Comment on the background quality.
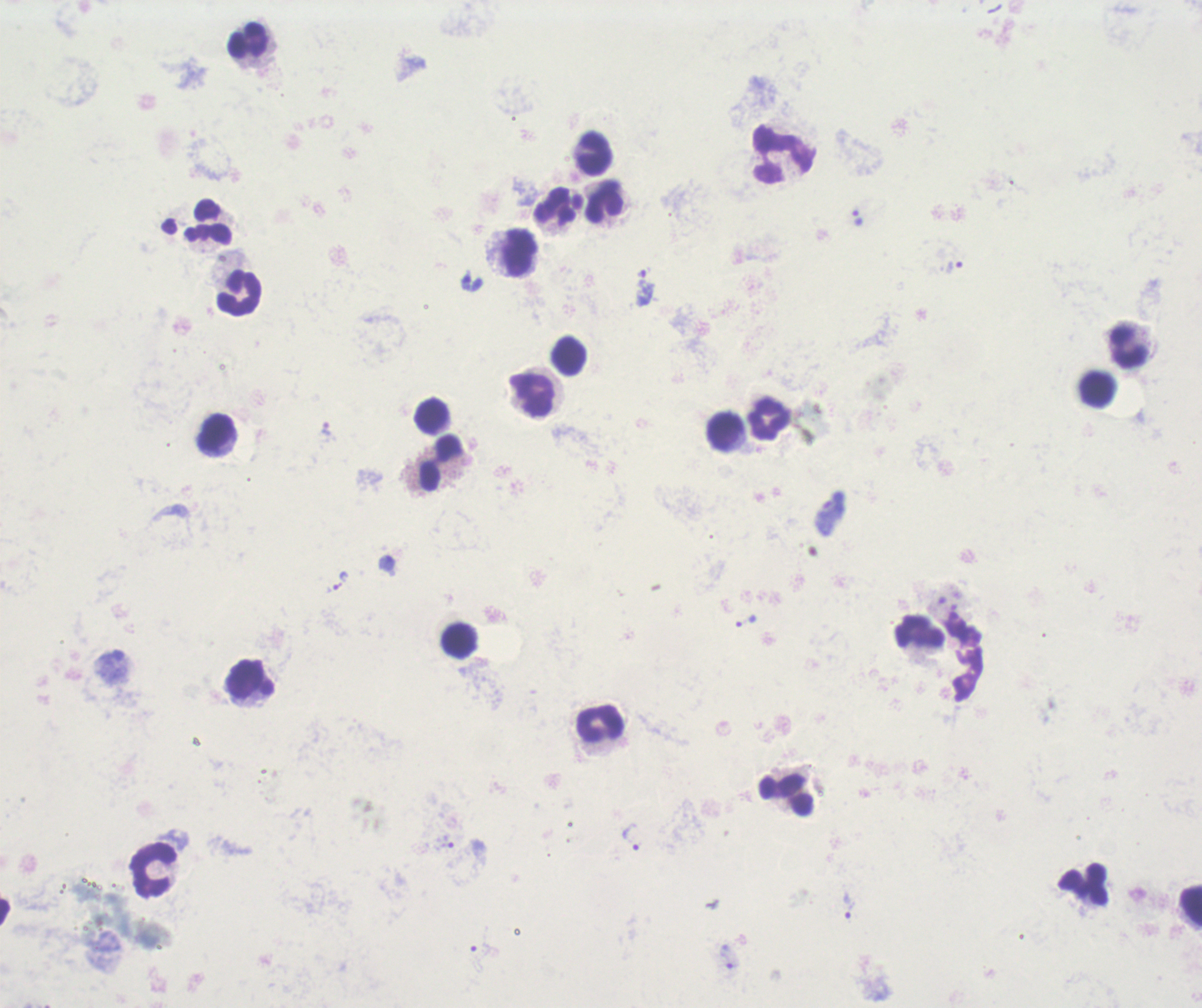
Poor.

Approximate centers as (x, y) in pixels.
Summary:
  - Trophozoite locations: (857, 218), (954, 266), (644, 288), (326, 428), (830, 514), (746, 620), (632, 838), (444, 842), (846, 908), (727, 956)
  - Leukocyte locations: (248, 39), (594, 152), (782, 153), (604, 201), (560, 205), (209, 222), (519, 250), (240, 292), (1128, 347), (569, 355), (1097, 390), (533, 395), (431, 416), (772, 418), (725, 431), (217, 433), (441, 461), (921, 632), (460, 642), (251, 679), (601, 723), (787, 796), (154, 870), (1084, 886), (1192, 904)
  - Stain: Romanowsky
  - Magnification: 100x
  - Field of view: one from this slide
  - Image size: 1202×1008 pixels
  - Preparation: thick blood film
  - Result: Plasmodium parasites identified
  - Context: previously used in an actual diagnosis